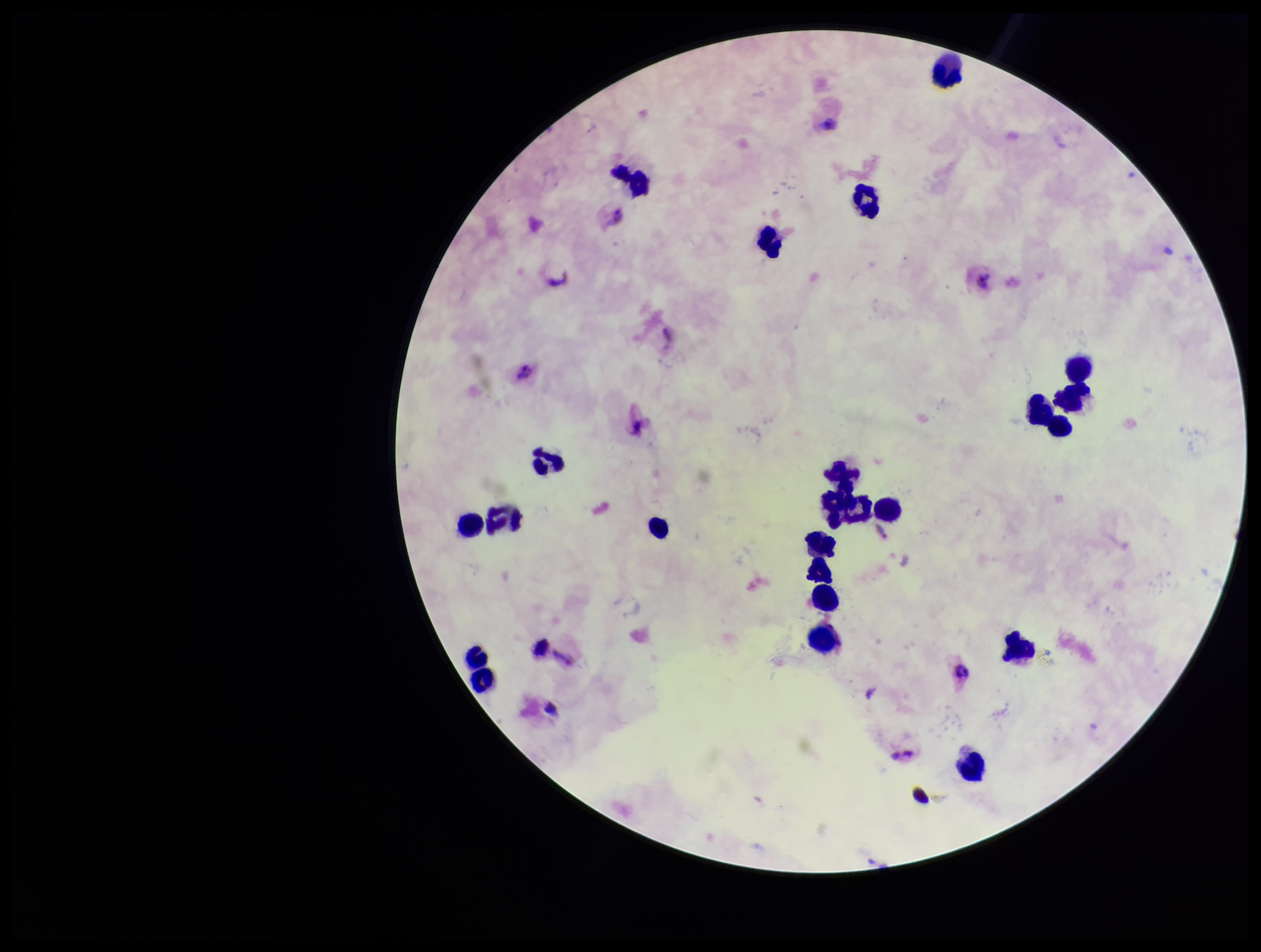

Summary:
  - Patient malaria status: infected
  - Stain: Giemsa
  - Capture: smartphone photograph through the microscope eyepiece
  - Species reported for this patient: Plasmodium vivax
  - Image size: 1261×952 pixels
  - Preparation: thick blood smear
  - Field of view: one from this slide
  - Parasite count: 1
  - Plasmodium parasites: detected
  - Leukocyte count: 20